Point out every Plasmodium parasite and every leukocyte.
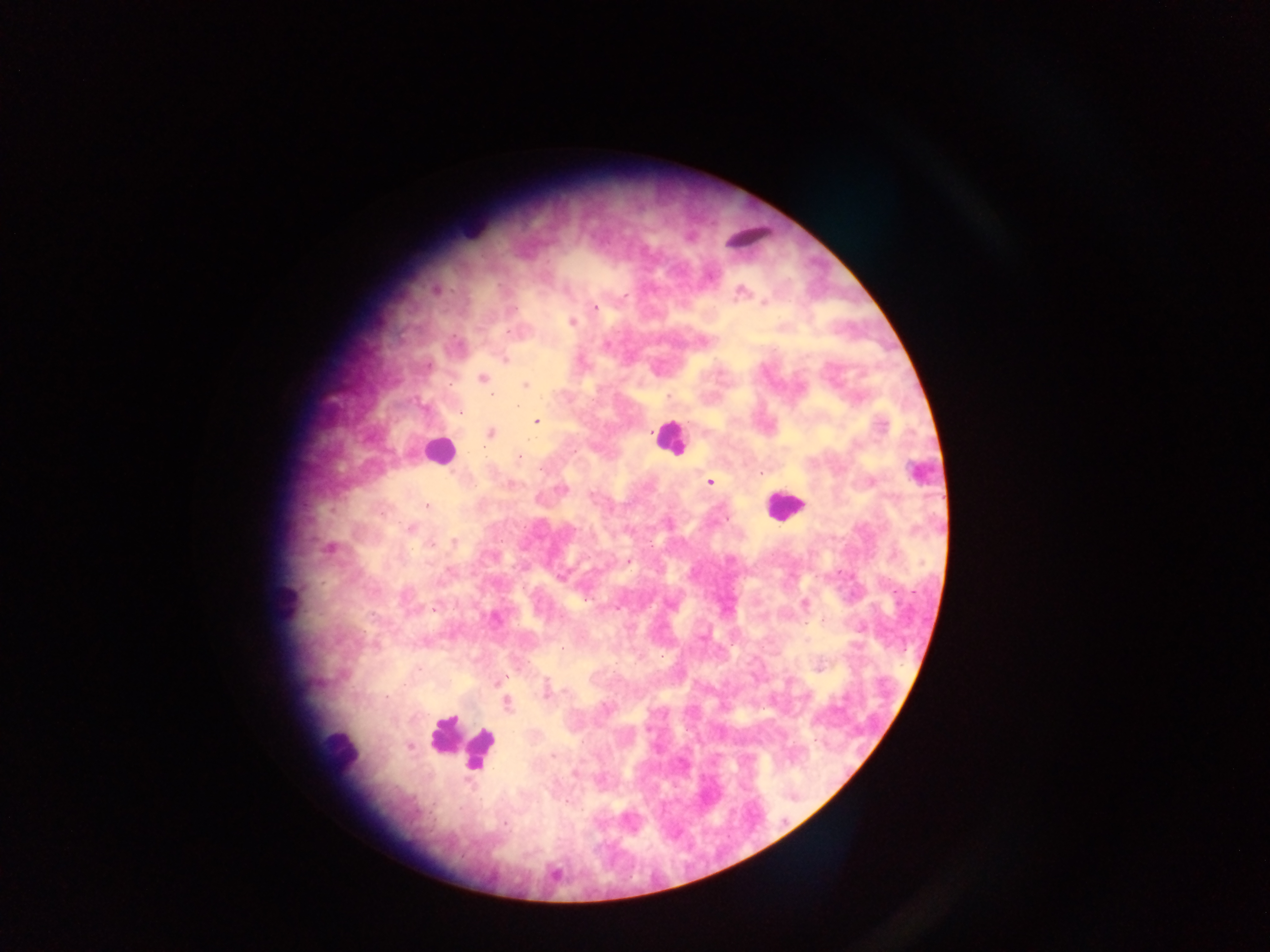
Approximate centers as (x, y) in pixels.
Plasmodium parasites: (595, 307), (571, 322), (525, 384), (450, 386), (492, 394), (461, 415), (534, 421), (490, 433), (518, 457), (708, 482), (424, 505), (409, 529), (452, 541), (819, 666).
Leukocytes: (666, 438), (444, 452), (787, 505), (342, 747).

Summary:
  - Image size: 1270×952 pixels
  - Preparation: thick blood smear
  - Country: Ghana
  - Capture: mobile-phone photograph through a microscope
  - Field of view: single